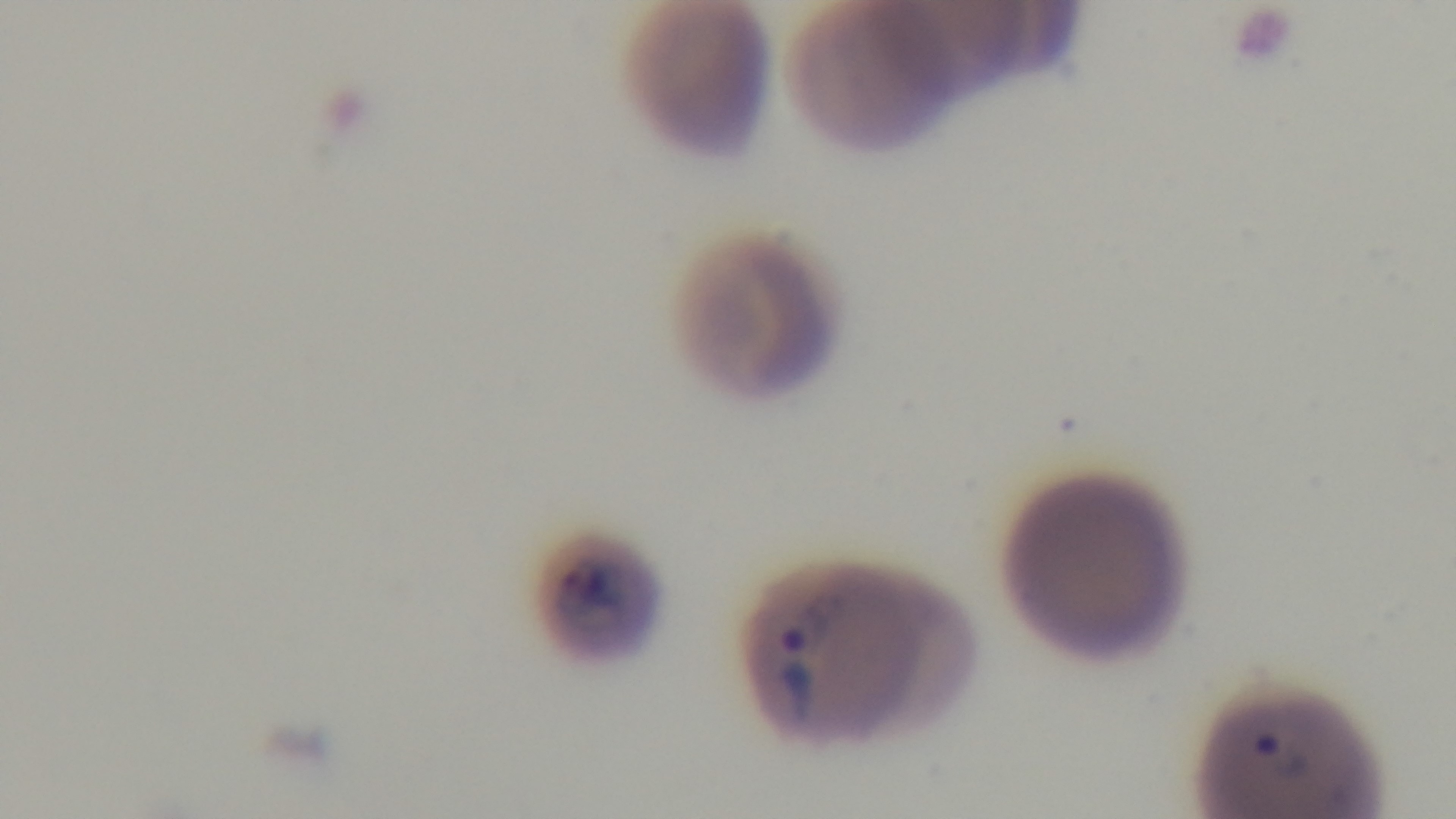

Summary:
  - Capture: mounted 4K digital camera
  - Objective: 100x oil immersion
  - Preparation: thin
  - Stain: Giemsa
  - Modality: light microscopy
  - Malaria status: positive
  - Field of view: one from the slide